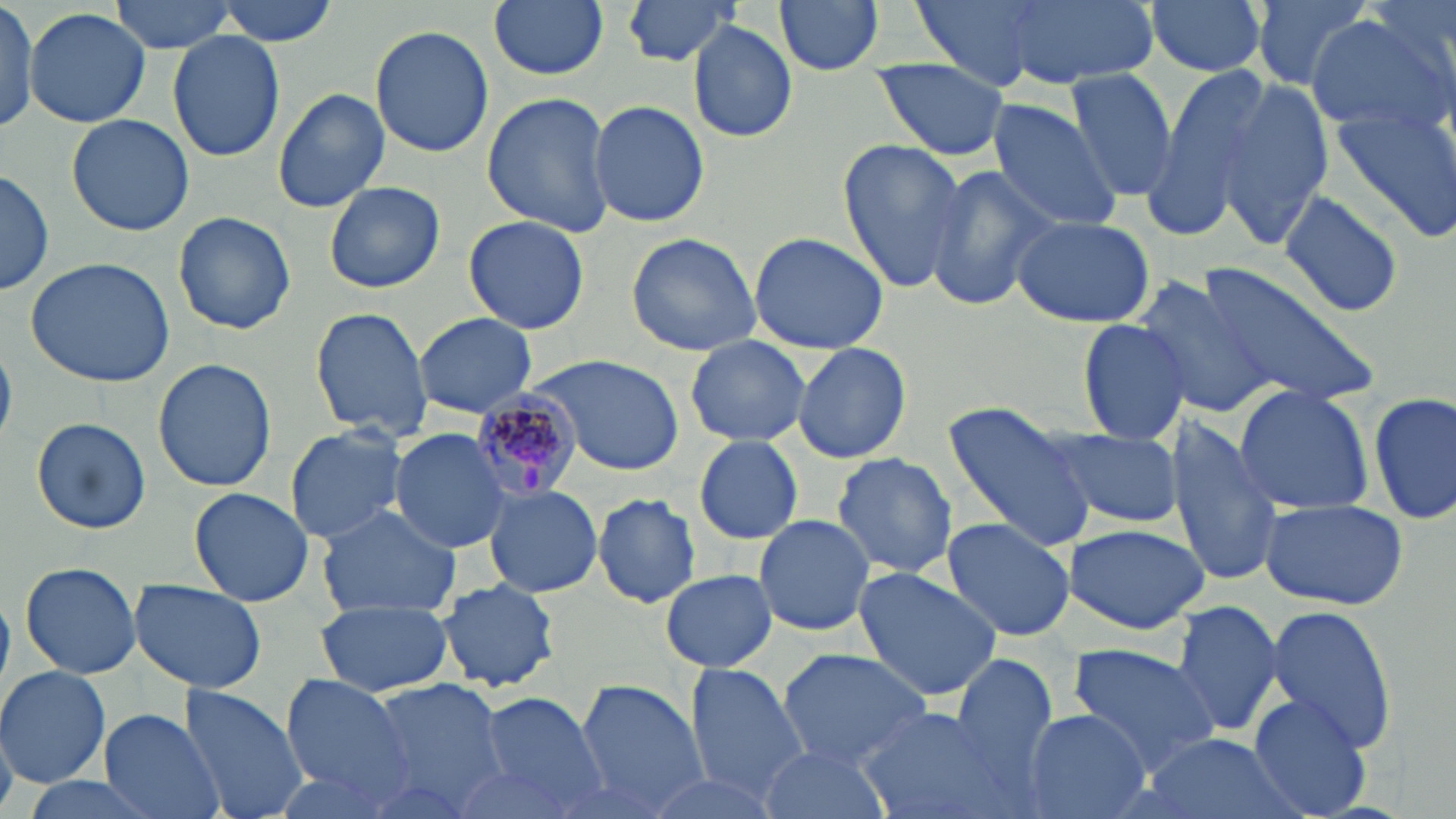

{
  "slide_level_diagnosis": "Plasmodium malariae",
  "modality": "light microscopy",
  "magnification": "1000x",
  "plasmodium_malariae_infected_red_blood_cell_locations": "approximate bounding boxes as (x1,y1)-(x2,y2) corner pairs in pixels: (469,388)-(588,500)",
  "preparation": "thin blood film",
  "uninfected_red_blood_cell_locations": "approximate bounding boxes as (x1,y1)-(x2,y2) corner pairs in pixels: (108,0)-(238,54), (214,0)-(339,45), (489,0)-(608,81), (620,0)-(740,66), (774,0)-(885,73), (911,0)-(1064,88), (1003,0)-(1156,88), (1147,0)-(1268,78), (1252,0)-(1379,94), (1364,0)-(1455,74), (0,2)-(38,135), (24,7)-(151,129), (1306,11)-(1450,131), (687,21)-(798,143), (371,23)-(493,158), (168,28)-(286,162), (872,58)-(1014,162), (1141,62)-(1279,227), (1064,66)-(1177,202), (1217,82)-(1335,250), (272,89)-(390,214), (481,92)-(617,238), (589,98)-(709,228), (985,101)-(1123,233), (1327,105)-(1456,244), (66,113)-(194,237), (837,140)-(965,294), (924,163)-(1058,313), (0,166)-(52,299), (324,180)-(446,295), (1280,187)-(1404,319), (172,210)-(296,336), (1010,212)-(1156,327), (462,215)-(590,335), (746,230)-(889,353), (625,232)-(763,357), (25,258)-(176,389), (1197,263)-(1384,411), (1132,274)-(1282,421), (308,305)-(434,441), (413,312)-(537,418), (1077,317)-(1192,446), (684,337)-(811,447), (790,342)-(912,464), (528,353)-(684,475), (153,356)-(275,492), (1234,385)-(1373,515), (1370,389)-(1454,525), (944,401)-(1097,553), (31,416)-(151,535), (1169,418)-(1282,586), (284,425)-(410,544), (387,427)-(515,553), (1049,430)-(1181,527), (694,435)-(805,545), (831,452)-(957,578), (483,482)-(603,600), (189,487)-(313,606), (591,493)-(700,609), (1258,499)-(1409,610), (313,504)-(464,618), (753,515)-(877,637), (940,516)-(1077,644), (1063,523)-(1207,634), (19,561)-(143,680), (851,567)-(1002,702), (661,568)-(777,672), (128,579)-(267,693), (436,581)-(562,693), (315,598)-(453,697), (1170,601)-(1285,737), (1265,605)-(1398,751), (1065,644)-(1221,776), (775,649)-(934,769), (949,653)-(1059,782), (685,664)-(810,800), (0,665)-(112,789), (280,675)-(412,798), (361,679)-(511,815), (575,680)-(708,816), (178,685)-(306,819), (475,692)-(612,816), (1246,694)-(1375,818), (99,706)-(226,819), (855,707)-(1012,819), (1019,708)-(1153,819), (1138,733)-(1297,819), (756,743)-(892,819), (450,760)-(587,819), (636,770)-(783,819), (16,776)-(159,819)",
  "stain": "May-Grünwald-Giemsa",
  "image_size": "1456×819 pixels",
  "field_of_view": "single"
}